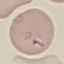 Malaria status: parasitized. Thin smear of blood. Photographed with a smartphone camera at the microscope eyepiece. Cell patch, automatically extracted from a larger field of view and resized to 64 × 64 pixels. Giemsa stain.